Assess this cell for malaria.
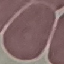
It is uninfected.

preparation: thin blood smear
image_type: cell patch, automatically extracted from a larger field of view and resized to 64 × 64 pixels
capture: smartphone camera at the microscope eyepiece
stain: Giemsa